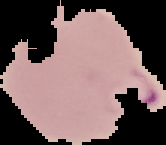
image_size: 166×145 pixels
preparation: thin blood smear
image_type: cell region segmented out of the field of view; surrounding area masked to black
malaria_status: parasitized